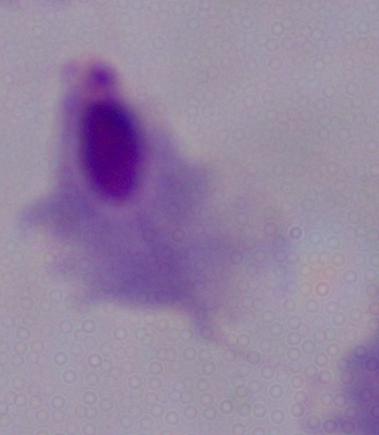
Captured at 1000x magnification. A trichomonad is shown. Photomicrograph.